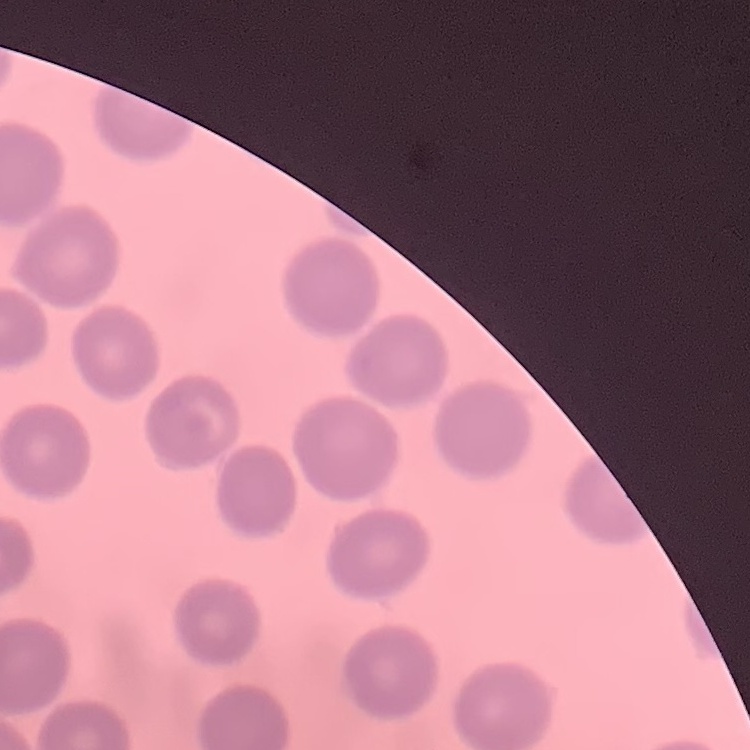

The erythrocytes exhibit no rouleaux formation. Field's or Giemsa stain. Square crop of a larger photomicrograph. Thin blood film.